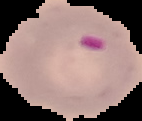
Segmented cell region on a black background. From a thin blood smear. Image is 142×121 pixels. Result: Plasmodium parasites detected.